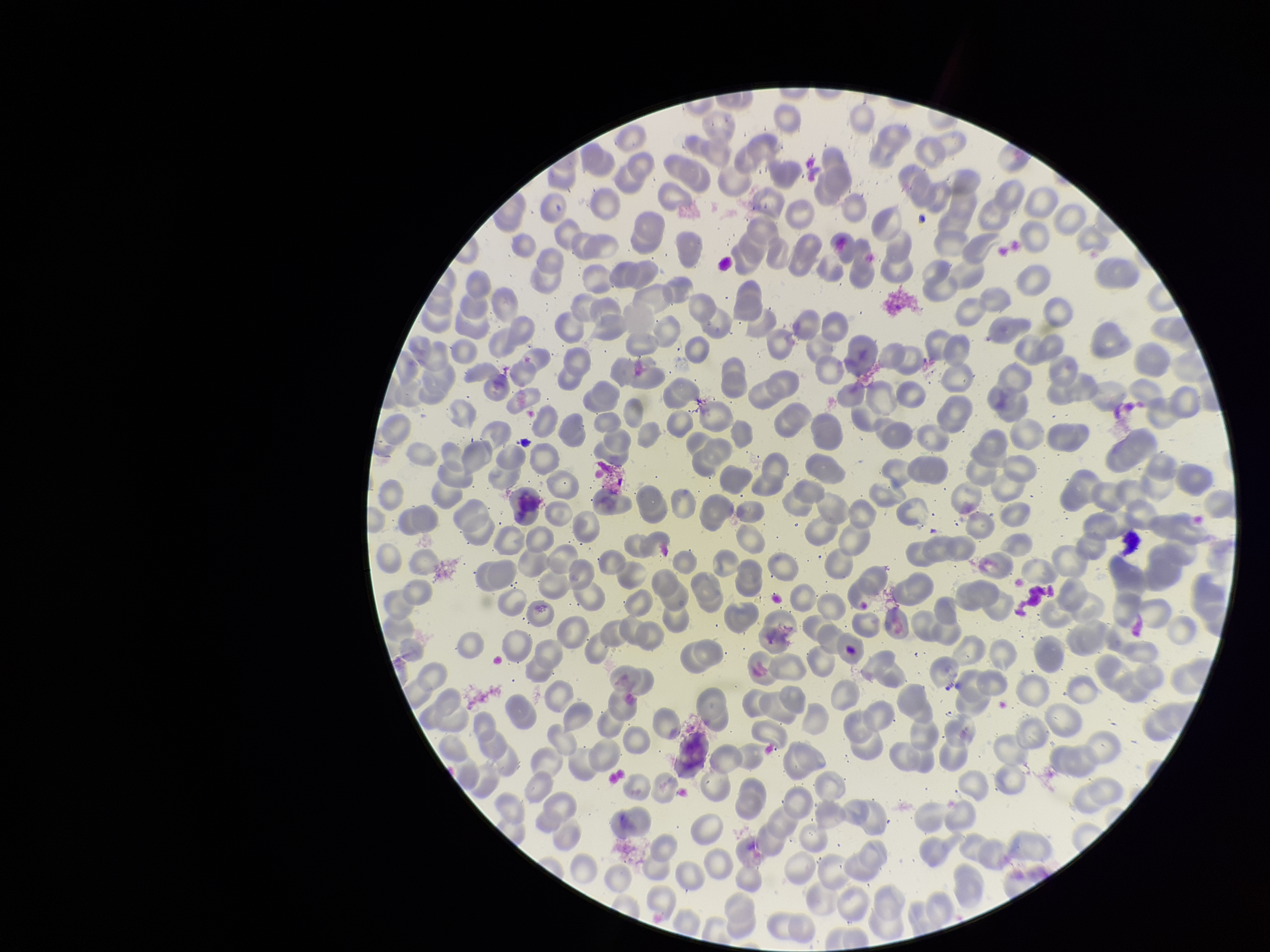

capture: smartphone photograph through the microscope eyepiece
stain: Giemsa
parasitized_red_blood_cell_count: 0
image_size: 1270×952 pixels
red_blood_cell_count: 295
patient_malaria_status: negative
field_of_view: single
parasitized_red_blood_cells: none identified
preparation: thin